Outline each uninfected red blood cell.
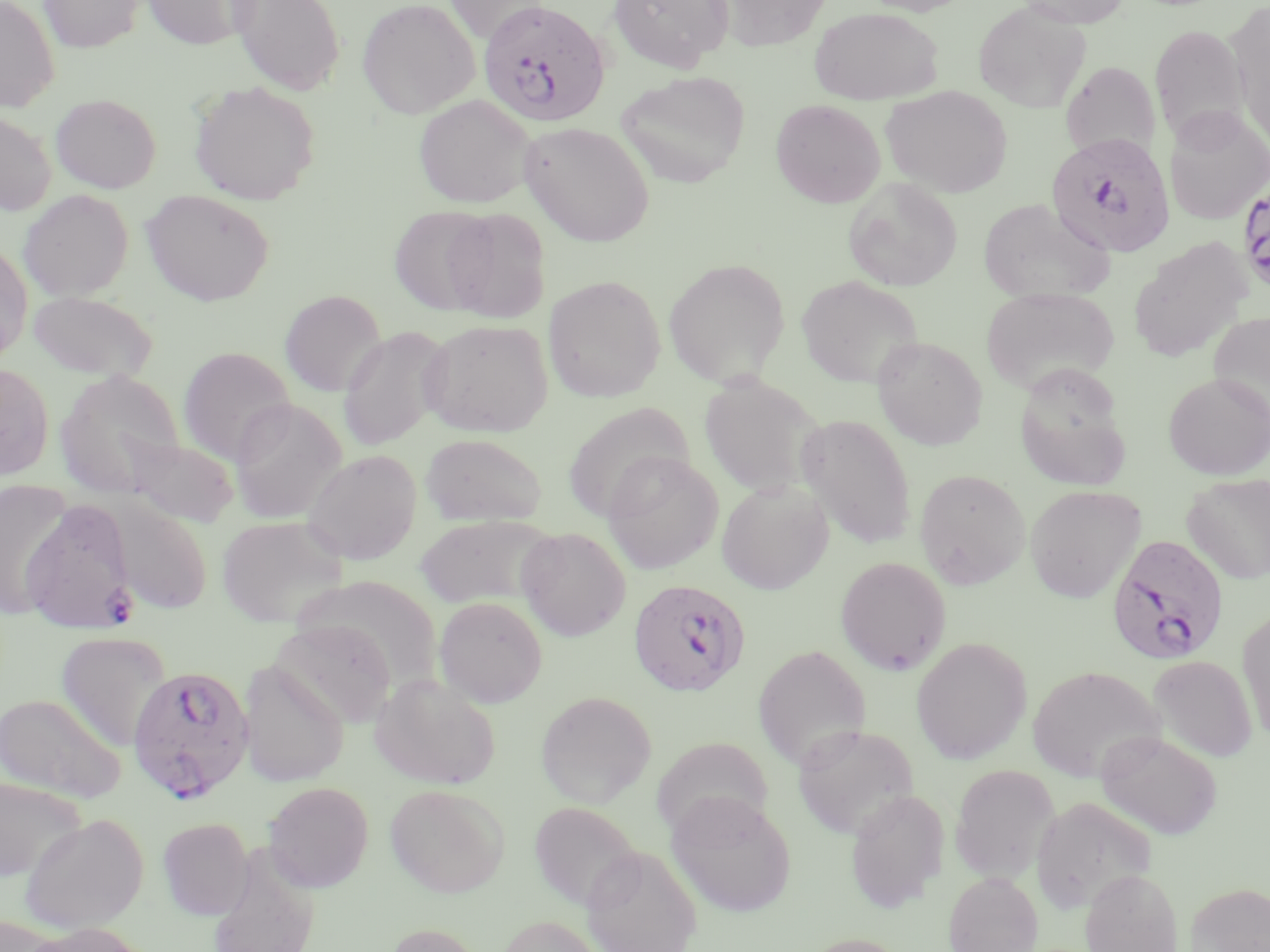

Approximate bounding boxes as (x1,y1)-(x2,y2) corner pairs in pixels.
Uninfected red blood cells: (0,0)-(60,112), (39,0)-(142,53), (142,0)-(257,49), (229,0)-(345,96), (357,0)-(479,118), (443,0)-(551,43), (609,0)-(733,72), (853,0)-(976,16), (1015,0)-(1133,28), (719,1)-(832,51), (974,1)-(1092,113), (1228,4)-(1270,146), (809,7)-(943,105), (1150,24)-(1249,142), (1060,61)-(1160,162), (616,70)-(751,188), (190,82)-(320,205), (881,85)-(1012,198), (51,93)-(161,193), (414,95)-(536,208), (771,99)-(885,208), (1163,106)-(1270,226), (0,110)-(56,216), (519,122)-(654,246), (843,177)-(962,291), (18,189)-(133,301), (141,190)-(274,306), (978,198)-(1112,303), (389,205)-(496,314), (443,207)-(551,323), (1128,238)-(1252,362), (0,242)-(33,363), (663,258)-(791,387), (543,275)-(665,403), (796,276)-(923,389), (981,286)-(1120,395), (27,290)-(158,382), (280,290)-(386,396), (1208,311)-(1270,424), (420,319)-(553,437), (337,325)-(453,452), (872,336)-(988,450), (178,347)-(296,465), (0,364)-(54,480), (56,369)-(186,497), (1163,373)-(1270,480), (699,374)-(825,499), (1018,385)-(1132,493), (228,398)-(347,524), (562,402)-(696,522), (797,413)-(917,549), (420,433)-(547,526), (121,436)-(240,528), (301,449)-(422,565), (602,451)-(723,574), (913,468)-(1030,589), (1183,472)-(1270,584), (716,478)-(834,594), (0,480)-(74,619), (1024,485)-(1145,603), (107,498)-(213,614), (415,514)-(555,609), (216,515)-(348,628), (517,527)-(631,641), (835,556)-(951,675), (298,576)-(443,684), (434,596)-(548,707), (1237,609)-(1270,743), (271,619)-(398,728), (55,631)-(170,751), (911,636)-(1032,764), (752,643)-(871,771), (1148,655)-(1257,763), (237,661)-(349,787), (1027,665)-(1165,783), (370,673)-(501,789), (536,691)-(657,806), (0,692)-(126,803), (791,724)-(920,839), (1096,730)-(1223,841), (651,736)-(774,839), (949,763)-(1060,884), (0,776)-(86,882), (263,781)-(374,892), (385,784)-(510,897), (845,788)-(949,913), (667,790)-(798,917), (1031,795)-(1157,914), (529,800)-(643,912), (19,813)-(149,934), (158,817)-(253,919), (581,845)-(702,952), (207,846)-(321,952), (1080,867)-(1184,952), (944,871)-(1043,952), (1185,881)-(1270,952), (496,915)-(606,952), (0,916)-(60,952), (26,922)-(152,952), (383,922)-(486,952), (800,933)-(910,952).

Summary:
  - Plasmodium falciparum-infected red blood cell locations: (478,4)-(610,130), (1045,131)-(1176,258), (1243,182)-(1270,287), (21,499)-(137,633), (1106,534)-(1230,666), (628,579)-(751,697), (127,664)-(255,804)
  - Slide-level diagnosis: Plasmodium falciparum
  - Stain: May-Grünwald-Giemsa
  - Field of view: one of a larger specimen
  - Magnification: 1000x
  - Preparation: thin blood film
  - Modality: light microscopy
  - Image size: 1270×952 pixels